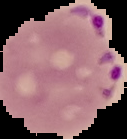
result = Plasmodium parasites identified
image type = segmented cell region with the area outside set to black
preparation = thin blood smear
image size = 127×139 pixels